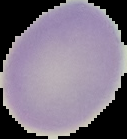

preparation = thin blood smear
image type = segmented cell region on a black background
image size = 127×139 pixels
malaria status = uninfected